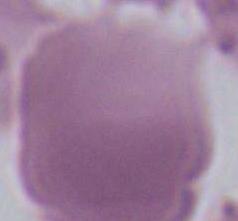

An erythrocyte is shown. 1000x magnification. Micrograph.